Classify this cell by malaria status.
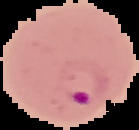

It is parasitized.

image size = 139×130 pixels
image type = segmented cell region on a black background
preparation = thin blood film